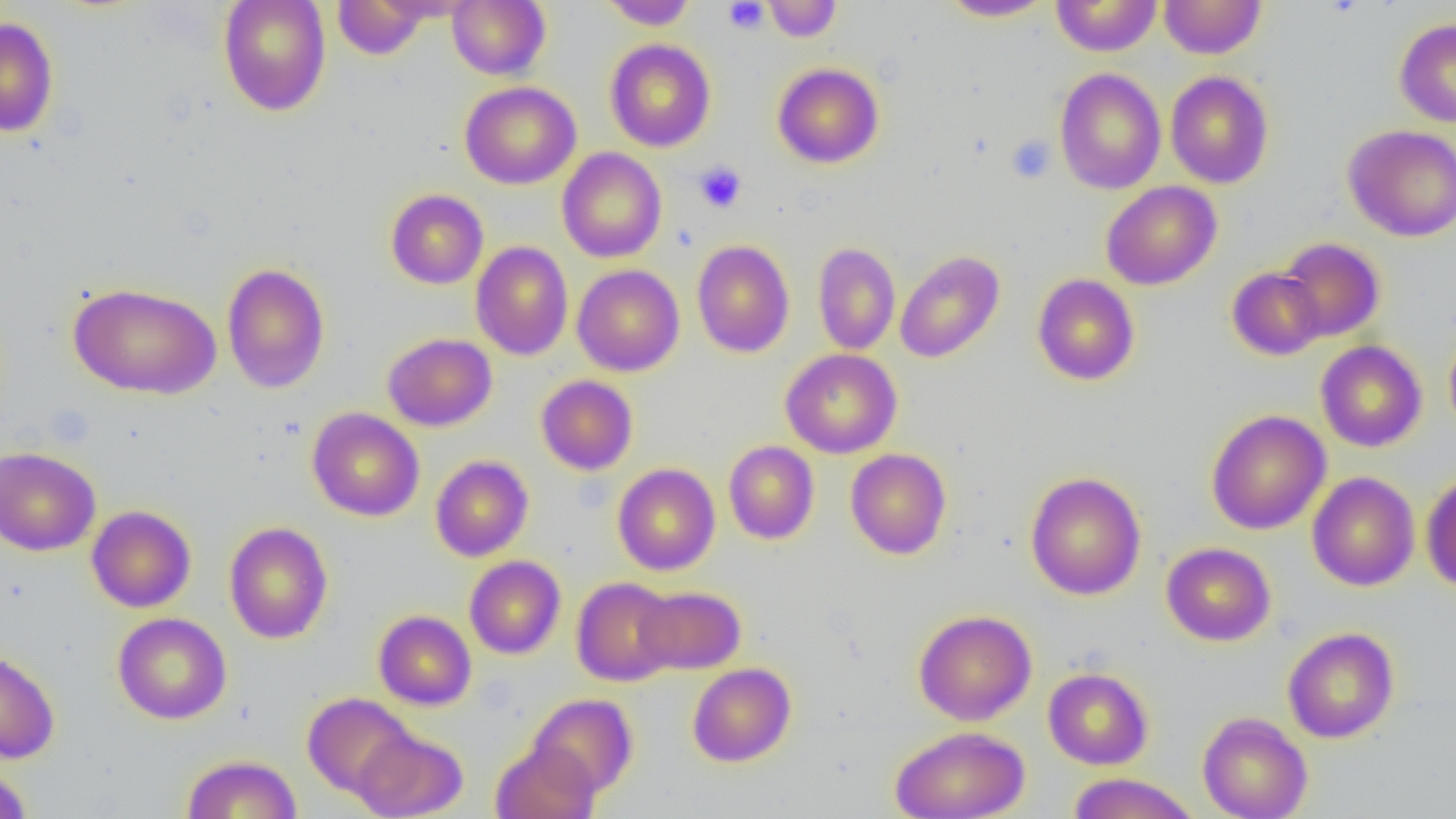

{
  "slide_level_diagnosis": "no evidence of blood parasites",
  "magnification": "1000x",
  "preparation": "thin blood smear",
  "uninfected_red_blood_cell_locations": "approximate bounding boxes as (x1, y1, x2, y2) in pixels: (218, 0, 331, 116), (332, 0, 431, 59), (447, 0, 550, 80), (764, 0, 841, 42), (942, 0, 1054, 21), (1050, 0, 1162, 56), (1159, 0, 1266, 59), (600, 1, 697, 30), (0, 17, 59, 137), (1394, 18, 1456, 127), (605, 39, 716, 152), (772, 63, 884, 168), (1054, 68, 1166, 194), (1165, 71, 1274, 188), (460, 81, 581, 189), (1343, 124, 1456, 242), (557, 147, 667, 263), (1101, 181, 1222, 290), (386, 189, 488, 289), (1278, 237, 1385, 342), (692, 240, 795, 357), (471, 241, 573, 360), (813, 242, 901, 356), (895, 250, 1005, 363), (222, 262, 330, 394), (572, 264, 684, 376), (1227, 267, 1326, 361), (1032, 274, 1140, 385), (67, 283, 221, 399), (1444, 322, 1456, 442), (382, 333, 497, 431), (1315, 341, 1427, 452), (780, 348, 902, 458), (536, 375, 638, 475), (307, 407, 424, 521), (1206, 410, 1331, 535), (723, 441, 820, 545), (0, 446, 101, 556), (845, 448, 951, 559), (430, 455, 534, 562), (612, 463, 720, 575), (1025, 471, 1146, 600), (1307, 471, 1420, 591), (1421, 471, 1456, 593), (86, 505, 196, 612), (224, 522, 333, 644), (1161, 542, 1276, 646), (464, 555, 566, 659), (571, 577, 679, 686), (635, 586, 746, 674), (913, 609, 1037, 725), (373, 610, 476, 710), (113, 612, 232, 724), (1282, 627, 1400, 743), (0, 648, 60, 763), (687, 662, 796, 767), (1043, 667, 1153, 770), (302, 692, 416, 798), (528, 693, 638, 799), (1197, 711, 1313, 819), (889, 725, 1031, 819), (353, 727, 467, 819), (491, 741, 600, 819), (182, 754, 302, 818), (0, 762, 34, 819), (1067, 772, 1199, 818)",
  "platelet_locations": "approximate bounding boxes as (x1, y1, x2, y2) in pixels: (723, 1, 769, 34), (1005, 135, 1056, 184), (694, 162, 747, 213)",
  "modality": "optical microscopy",
  "field_of_view": "single",
  "image_size": "1456×819 pixels"
}